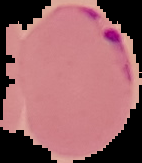
Malaria status: parasitized. From a thin blood smear. Image is 142×163 pixels. Segmented cell region on a black background.